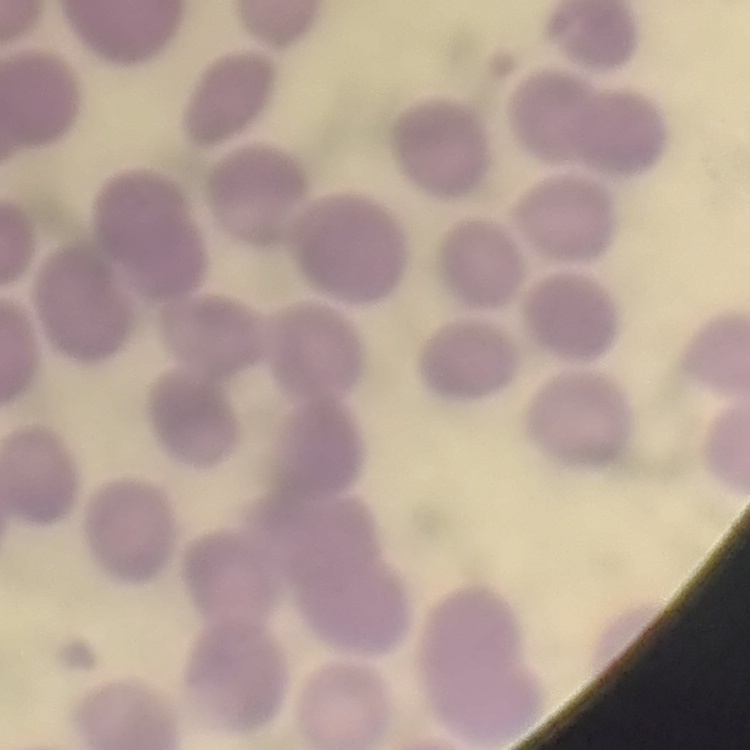
The erythrocytes show no rouleaux formation. Square crop of a larger photomicrograph. Thin blood film. Stained with either Field's or Giemsa.